Describe the morphology of the red blood cells.
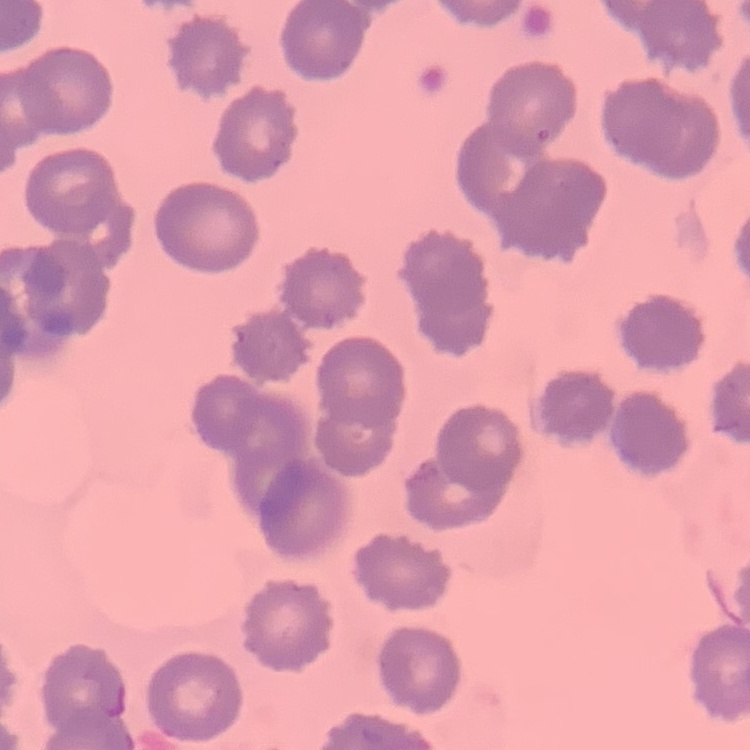

They show no rouleaux formation.

{
  "stain": "Field's or Giemsa",
  "image_type": "square crop of a larger photomicrograph",
  "preparation": "thin peripheral smear"
}